Comment on the morphology of the erythrocytes.
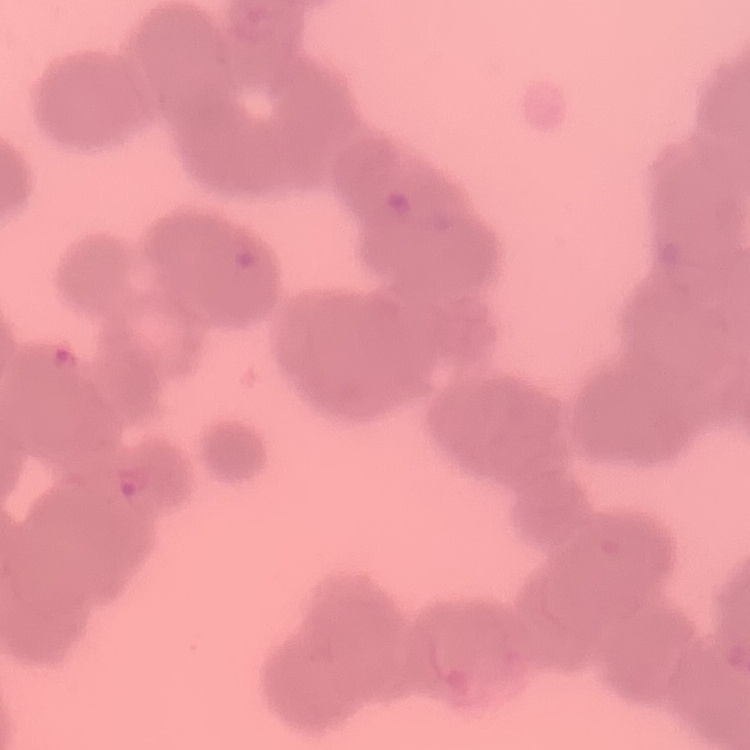

They show rouleaux formation.

preparation: thin blood film
image_type: one tile cut from a larger photomicrograph
stain: Field's or Giemsa